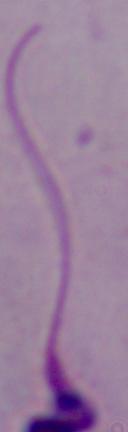
Summary:
  - Magnification: 1000x
  - Identification: Leishmania
  - Modality: micrograph